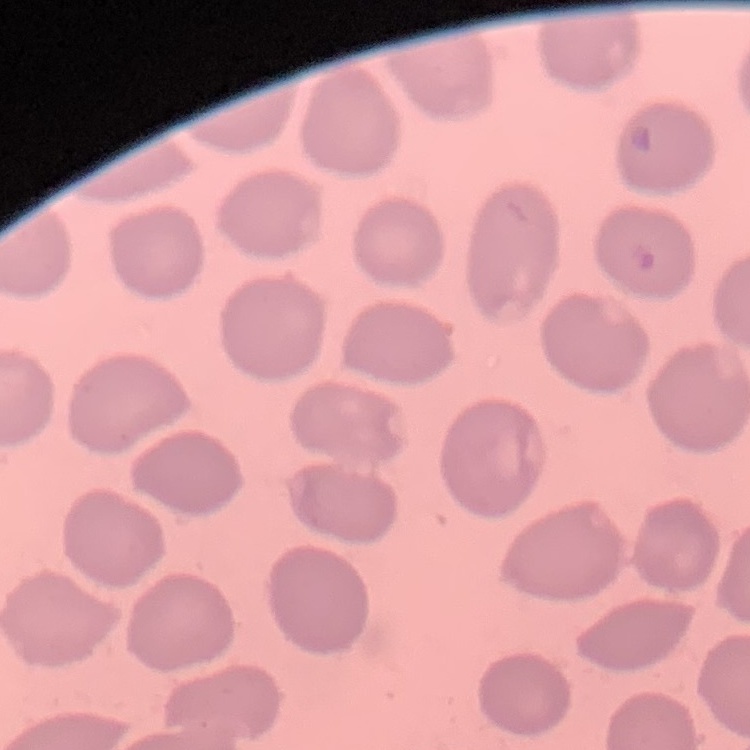
red blood cell morphology = no rouleaux formation
image type = square crop of a larger photomicrograph
preparation = thin peripheral smear
stain = Field's or Giemsa